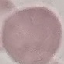
Summary:
  - Malaria status: uninfected
  - Capture: smartphone camera at the microscope eyepiece
  - Stain: Giemsa
  - Image type: automatically extracted cell patch, resized to 64 × 64 pixels
  - Preparation: thin smear